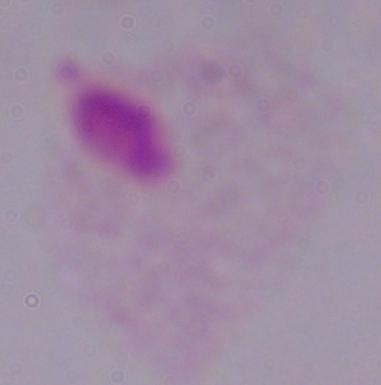
A trichomonad is shown. Captured at 1000x magnification. Micrograph.